Classify this cell by malaria status.
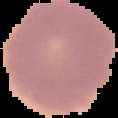

Uninfected.

preparation: thin blood film
image_type: segmented cell region on a black background
image_size: 118×118 pixels